Classify this cell by malaria status.
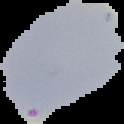
Uninfected.

Summary:
  - Image type: segmented cell region with the area outside set to black
  - Image size: 124×124 pixels
  - Preparation: thin blood film